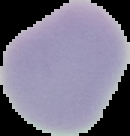
From a thin blood film. The area outside the segmented cell region is set to black. Image is 130×136 pixels. Malaria status: uninfected.